Comment on the morphology of the red blood cells.
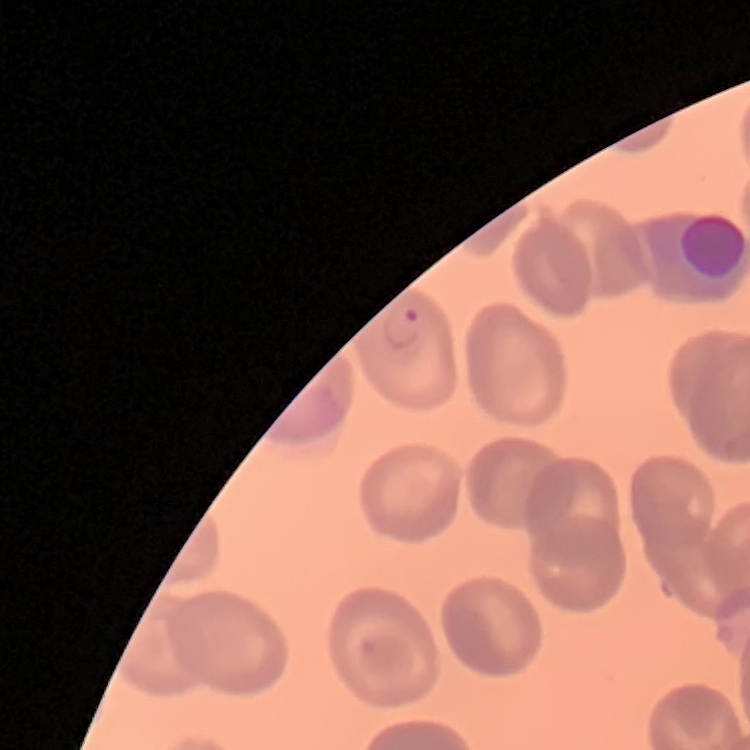

No rouleaux formation.

Stained with either Field's or Giemsa. One tile cut from a larger photomicrograph. Thin peripheral smear.